State which parasite is depicted.
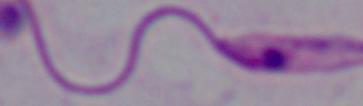
This is Leishmania.

Summary:
  - Magnification: 1000x
  - Modality: photomicrograph